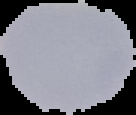
Summary:
  - Preparation: thin blood smear
  - Malaria status: uninfected
  - Image size: 136×115 pixels
  - Image type: segmented cell region with the area outside set to black